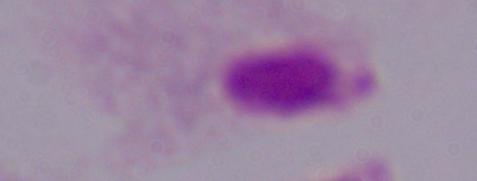
magnification = 1000x
identification = trichomonad
modality = photomicrograph